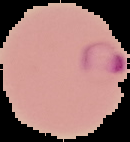
image size = 130×142 pixels
preparation = thin blood smear
image type = cell region segmented out of the field of view; surrounding area masked to black
malaria status = parasitized